Locate and identify every blood parasite.
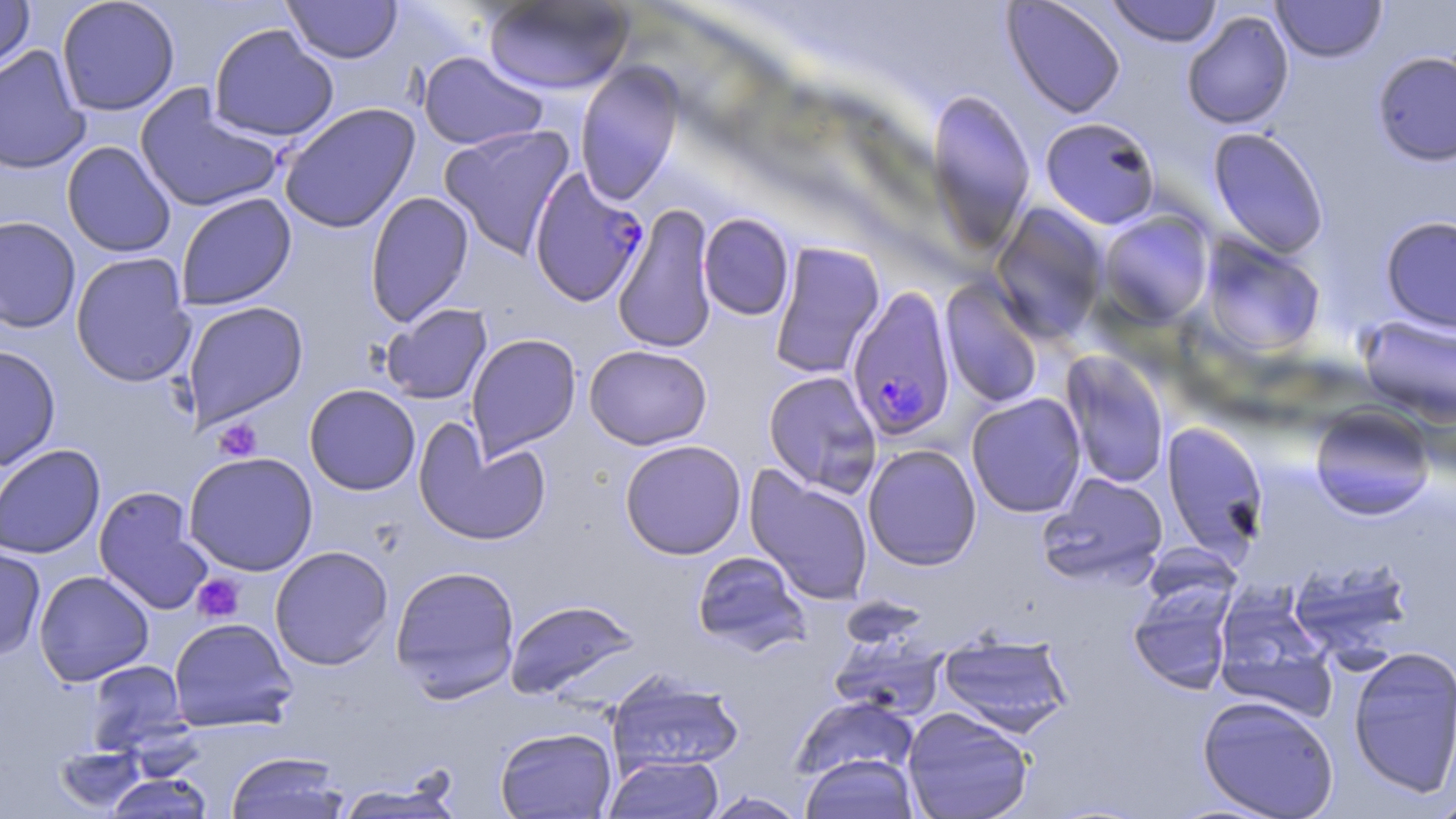
Approximate bounding boxes as (x1,y1)-(x2,y2) corner pairs in pixels.
Plasmodium falciparum-infected red blood cells: (528,166)-(649,307), (846,285)-(957,441).
No Plasmodium ovale, Plasmodium malariae, Plasmodium vivax, Babesia divergens, or Trypanosoma brucei observed.

{
  "slide_level_diagnosis": "Plasmodium falciparum",
  "stain": "May-Grünwald-Giemsa",
  "field_of_view": "single",
  "modality": "light microscopy",
  "preparation": "thin blood smear",
  "magnification": "1000x",
  "platelet_locations": "approximate bounding boxes as (x1,y1)-(x2,y2) corner pairs in pixels: (212,419)-(263,461), (192,574)-(245,624)",
  "image_size": "1456×819 pixels",
  "uninfected_red_blood_cell_locations": "approximate bounding boxes as (x1,y1)-(x2,y2) corner pairs in pixels: (0,0)-(35,75), (56,0)-(180,116), (283,0)-(402,64), (1105,0)-(1224,47), (483,1)-(634,95), (1002,1)-(1126,119), (1271,1)-(1387,63), (1181,10)-(1294,130), (208,24)-(340,143), (0,45)-(91,175), (1372,50)-(1456,166), (417,51)-(550,151), (575,63)-(683,204), (134,85)-(284,214), (926,88)-(1036,251), (277,103)-(420,234), (1040,116)-(1161,230), (439,124)-(575,260), (1208,127)-(1330,259), (61,141)-(176,258), (365,191)-(474,327), (175,193)-(297,311), (990,203)-(1108,345), (613,204)-(718,354), (1098,211)-(1214,327), (698,213)-(795,320), (0,215)-(82,334), (1380,215)-(1456,334), (1200,235)-(1326,357), (769,241)-(886,379), (70,252)-(196,387), (940,278)-(1044,409), (181,301)-(309,428), (380,303)-(493,405), (1357,315)-(1456,425), (466,333)-(582,459), (584,344)-(713,449), (0,345)-(60,472), (1061,351)-(1170,489), (762,370)-(883,497), (304,384)-(421,495), (966,393)-(1087,518), (1309,404)-(1436,520), (413,420)-(552,546), (1162,421)-(1269,559), (619,439)-(747,560), (0,443)-(106,559), (862,443)-(982,571), (183,451)-(319,576), (745,467)-(874,605), (1037,472)-(1169,588), (93,486)-(214,615), (0,544)-(46,660), (269,546)-(394,670), (691,551)-(810,655), (1288,557)-(1415,662), (389,564)-(521,701), (33,569)-(154,686), (1127,581)-(1237,695), (1213,587)-(1337,719), (505,598)-(641,701), (168,617)-(297,732), (828,633)-(949,721), (938,633)-(1074,737), (1347,645)-(1456,799), (85,660)-(189,754), (606,670)-(745,776), (791,695)-(918,783), (1197,695)-(1340,818), (901,706)-(1035,819), (494,726)-(617,818), (54,745)-(147,813), (225,751)-(351,819), (799,753)-(920,819), (603,755)-(724,818), (103,772)-(215,818), (334,779)-(466,818), (702,791)-(808,818), (1430,795)-(1456,819)"
}